Name the blood parasite species.
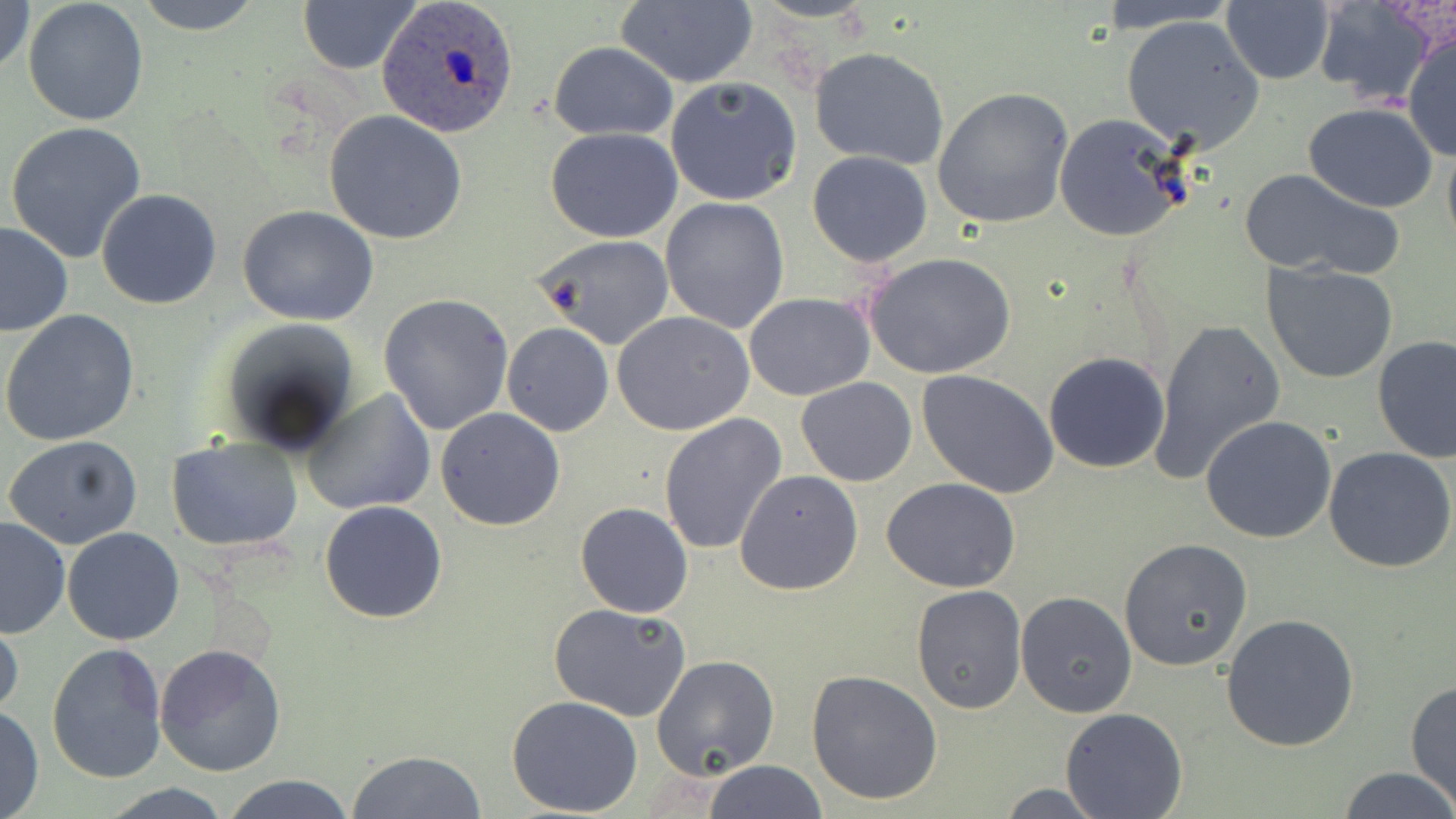

Plasmodium ovale.

image_size: 1456×819 pixels
plasmodium_ovale_infected_red_blood_cell_locations: 'approximate bounding boxes as named x1/y1/x2/y2 corners in pixels: (x1=377, y1=0, x2=518, y2=138)'
modality: light microscopy
preparation: thin blood smear
field_of_view: single
magnification: 1000x
stain: May-Grünwald-Giemsa
uninfected_red_blood_cell_locations: 'approximate bounding boxes as named x1/y1/x2/y2 corners in pixels: (x1=1, y1=0, x2=35, y2=84), (x1=134, y1=0, x2=265, y2=35), (x1=296, y1=0, x2=423, y2=74), (x1=612, y1=0, x2=757, y2=89), (x1=1093, y1=0, x2=1240, y2=31), (x1=1222, y1=0, x2=1336, y2=85), (x1=1312, y1=0, x2=1440, y2=106), (x1=23, y1=1, x2=149, y2=125), (x1=1121, y1=15, x2=1265, y2=153), (x1=1403, y1=29, x2=1456, y2=162), (x1=548, y1=41, x2=677, y2=141), (x1=808, y1=46, x2=950, y2=169), (x1=666, y1=76, x2=802, y2=205), (x1=932, y1=87, x2=1074, y2=231), (x1=1302, y1=102, x2=1439, y2=212), (x1=325, y1=111, x2=467, y2=246), (x1=1053, y1=112, x2=1194, y2=244), (x1=4, y1=121, x2=148, y2=263), (x1=545, y1=128, x2=683, y2=243), (x1=1442, y1=130, x2=1456, y2=258), (x1=807, y1=150, x2=933, y2=265), (x1=1238, y1=165, x2=1405, y2=280), (x1=96, y1=190, x2=223, y2=309), (x1=660, y1=196, x2=789, y2=334), (x1=237, y1=204, x2=379, y2=326), (x1=0, y1=221, x2=73, y2=337), (x1=531, y1=234, x2=675, y2=351), (x1=862, y1=251, x2=1016, y2=379), (x1=1260, y1=262, x2=1400, y2=384), (x1=743, y1=292, x2=876, y2=401), (x1=378, y1=293, x2=515, y2=435), (x1=0, y1=310, x2=140, y2=448), (x1=612, y1=310, x2=754, y2=435), (x1=214, y1=318, x2=360, y2=455), (x1=1147, y1=318, x2=1285, y2=487), (x1=501, y1=321, x2=615, y2=437), (x1=463, y1=333, x2=591, y2=486), (x1=1373, y1=336, x2=1455, y2=462), (x1=1043, y1=351, x2=1171, y2=474), (x1=917, y1=369, x2=1060, y2=499), (x1=797, y1=377, x2=917, y2=487), (x1=303, y1=388, x2=436, y2=516), (x1=435, y1=408, x2=566, y2=530), (x1=658, y1=413, x2=788, y2=558), (x1=1201, y1=415, x2=1337, y2=543), (x1=3, y1=436, x2=145, y2=551), (x1=167, y1=436, x2=304, y2=553), (x1=1324, y1=446, x2=1455, y2=573), (x1=30, y1=467, x2=165, y2=612), (x1=734, y1=468, x2=862, y2=596), (x1=882, y1=476, x2=1021, y2=593), (x1=320, y1=499, x2=450, y2=623), (x1=575, y1=501, x2=694, y2=618), (x1=1, y1=516, x2=71, y2=639), (x1=63, y1=528, x2=184, y2=645), (x1=1120, y1=537, x2=1254, y2=672), (x1=911, y1=585, x2=1028, y2=714), (x1=1016, y1=591, x2=1139, y2=718), (x1=549, y1=602, x2=692, y2=721), (x1=0, y1=613, x2=24, y2=727), (x1=1220, y1=613, x2=1361, y2=751), (x1=45, y1=641, x2=166, y2=784), (x1=155, y1=641, x2=287, y2=776), (x1=651, y1=654, x2=780, y2=779), (x1=805, y1=670, x2=943, y2=805), (x1=1405, y1=681, x2=1455, y2=808), (x1=505, y1=695, x2=644, y2=817), (x1=0, y1=704, x2=43, y2=818), (x1=1059, y1=708, x2=1187, y2=818), (x1=348, y1=749, x2=488, y2=819), (x1=702, y1=761, x2=827, y2=817), (x1=1335, y1=767, x2=1456, y2=819), (x1=218, y1=772, x2=359, y2=819), (x1=989, y1=781, x2=1114, y2=817), (x1=94, y1=784, x2=240, y2=817)'